Assess the morphology of the erythrocytes.
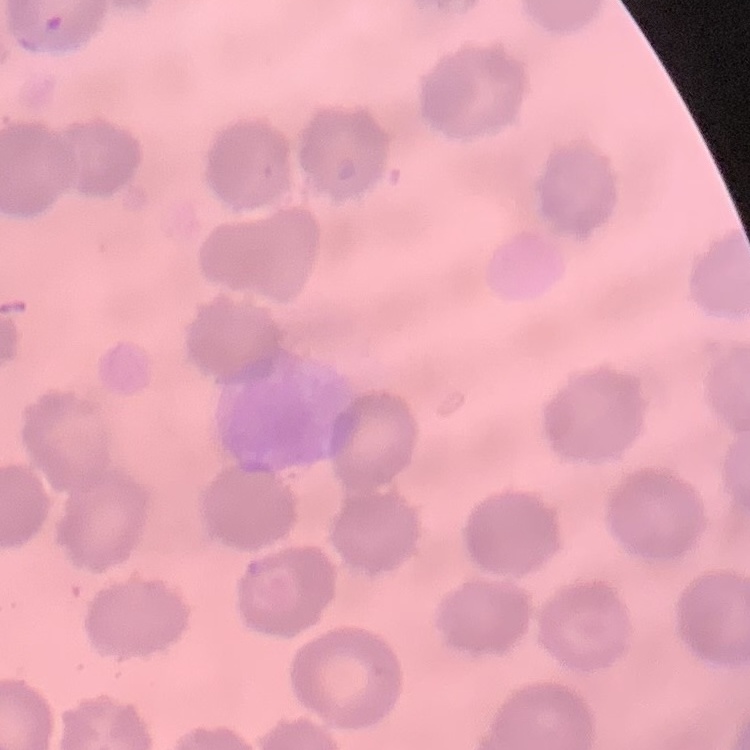
They show no rouleaux formation.

stain: Field's or Giemsa
preparation: thin peripheral smear
image_type: one tile cut from a larger photomicrograph